Locate and identify every blood parasite.
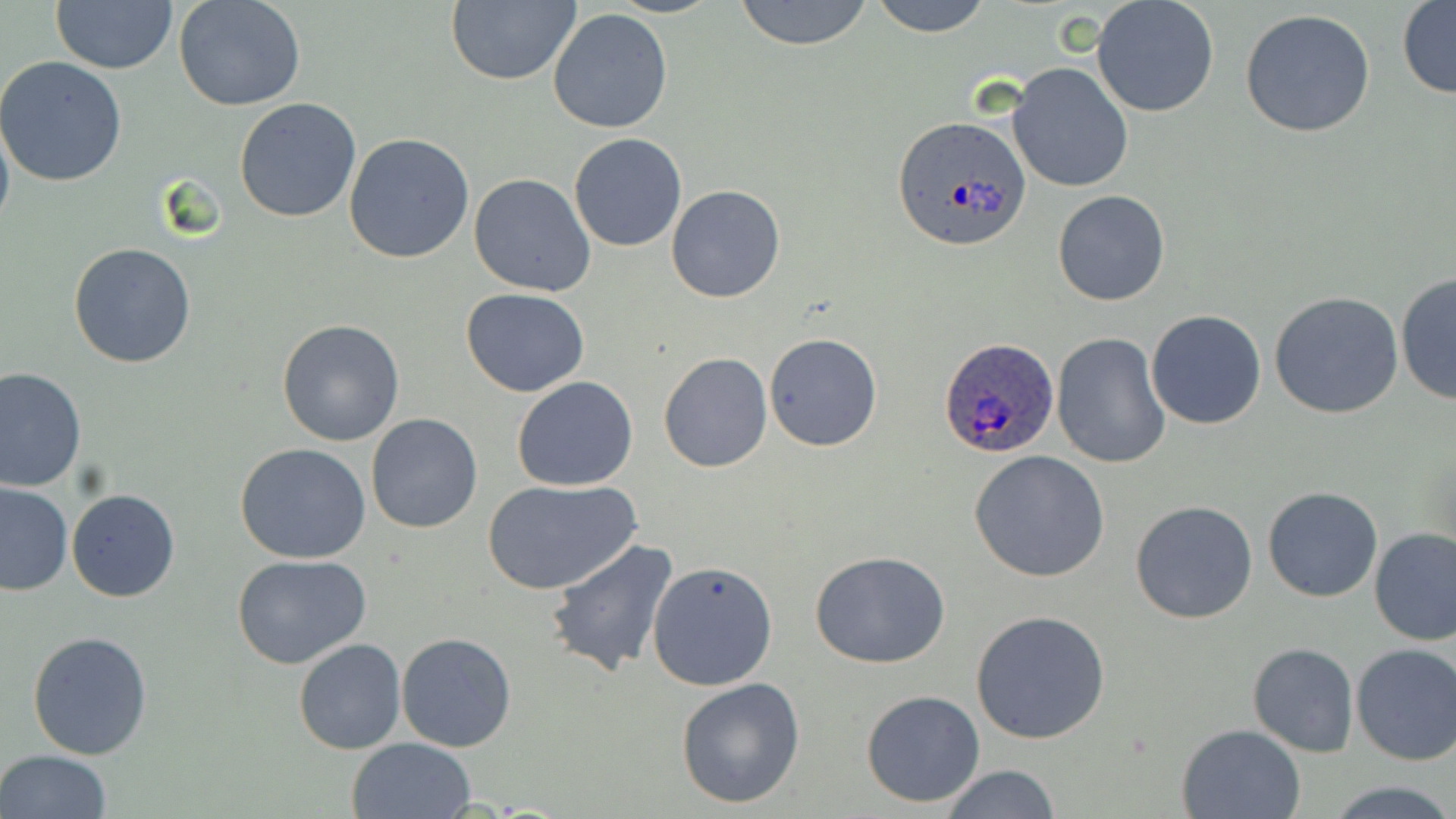

Approximate bounding boxes as [x1, y1, x2, y2] in pixels.
Plasmodium ovale-infected red blood cells: [888, 113, 1031, 252], [941, 337, 1060, 459].
No Plasmodium falciparum, Plasmodium malariae, Plasmodium vivax, Babesia divergens, or Trypanosoma brucei observed.

Uninfected red blood cell locations: [174, 0, 307, 111], [445, 0, 580, 87], [734, 0, 874, 50], [871, 0, 993, 37], [1091, 0, 1218, 118], [51, 1, 178, 75], [1397, 1, 1456, 98], [547, 8, 673, 134], [1240, 9, 1376, 139], [0, 56, 128, 187], [1007, 62, 1133, 192], [234, 99, 362, 223], [0, 103, 15, 242], [344, 132, 475, 263], [569, 134, 688, 253], [469, 172, 597, 296], [664, 184, 785, 303], [1053, 190, 1170, 306], [67, 243, 196, 368], [1394, 271, 1456, 406], [462, 288, 590, 397], [1269, 291, 1404, 419], [1147, 310, 1268, 429], [277, 318, 404, 447], [763, 332, 883, 452], [1052, 332, 1173, 469], [658, 352, 773, 474], [0, 367, 86, 494], [513, 376, 639, 491], [365, 413, 484, 533], [234, 444, 373, 565], [968, 450, 1110, 581], [483, 479, 639, 595], [0, 482, 73, 595], [1264, 487, 1382, 603], [67, 489, 180, 602], [1130, 499, 1260, 625], [1369, 526, 1456, 645], [546, 537, 679, 678], [809, 551, 953, 670], [231, 555, 373, 671], [648, 560, 779, 689], [971, 610, 1111, 744], [27, 631, 155, 760], [396, 633, 519, 752], [293, 638, 408, 755], [1247, 643, 1360, 757], [1352, 643, 1456, 766], [675, 676, 807, 810], [862, 689, 984, 808], [1176, 723, 1306, 818], [347, 738, 475, 819], [0, 750, 113, 819], [937, 764, 1060, 819], [1331, 782, 1455, 818]. Slide-level diagnosis: Plasmodium ovale. Image is 1456×819 pixels. Thin blood film. May-Grünwald-Giemsa stain. Optical microscopy. One field of a larger specimen. 1000x magnification.